Locate every malaria parasite.
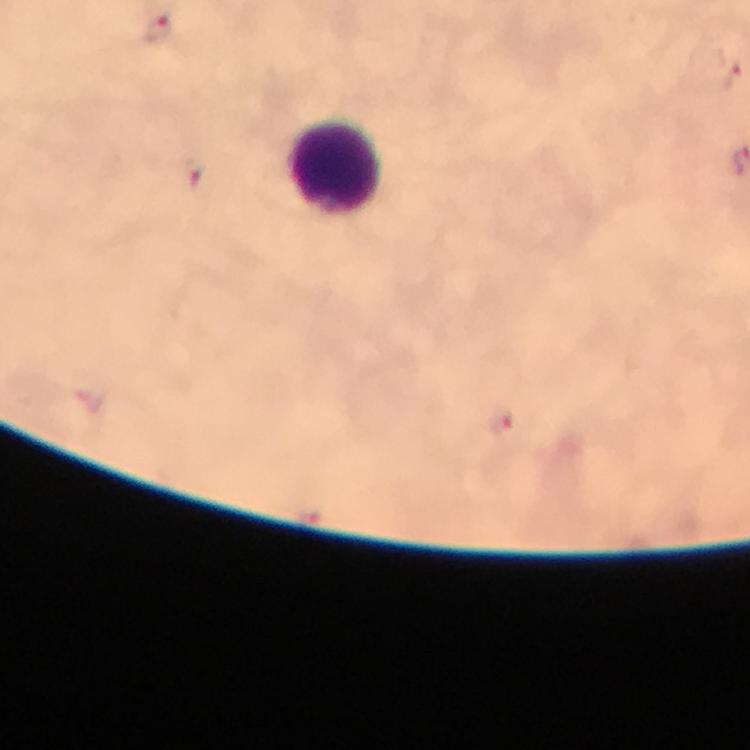

Approximate centers as [x, y] in pixels.
Malaria parasites: [155, 31], [730, 74], [503, 426].

Summary:
  - Leukocyte locations: [336, 167]
  - Stain: Giemsa
  - Preparation: thick blood smear
  - Immersion oil: applied
  - Context: from a malaria diagnostic workup
  - Cropped from: a single field of view
  - Capture: smartphone camera through the microscope
  - Magnification: 100x
  - Image size: 750×750 pixels